Give the position of each P. falciparum parasite with its life-cycle stage, each leukocyte, and any debris.
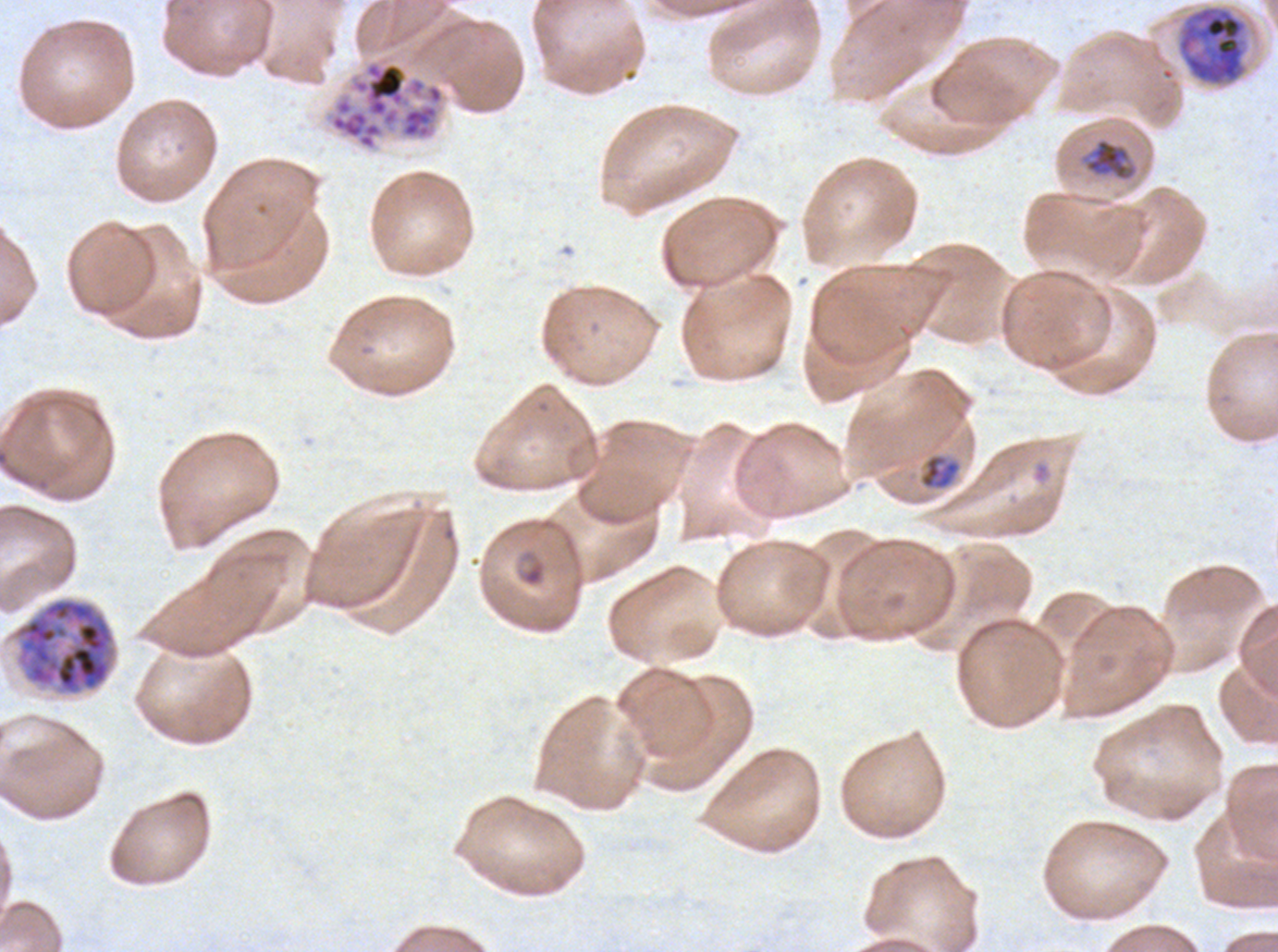

Approximate bounding rectangles given as corner coordinates in pixels from the top-left.
Rings: (x1=515, y1=547, x2=548, y2=588).
Late-ring/early-trophozoite forms: (x1=918, y1=453, x2=962, y2=491).
Mid trophozoites: (x1=1085, y1=138, x2=1132, y2=181).
Early schizonts: (x1=1176, y1=4, x2=1248, y2=87).
Late schizonts: (x1=12, y1=597, x2=117, y2=696).
Segmenters: (x1=325, y1=55, x2=447, y2=153).
No late trophozoites, gametocytes, leukocytes, or debris observed.

Image is 1278×952 pixels. Giemsa stain. Life-cycle stages observed: ring, late-ring/early-trophozoite, mid trophozoite, early schizont, late schizont, segmenter. A sub-image separated from a larger composite. Thin blood smear. Ex-vivo P. falciparum culture from a patient in The Gambia, grown for 24 to 48 hours.